Classify this cell by malaria status.
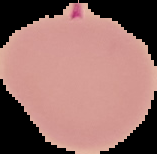

It is parasitized.

Summary:
  - Preparation: thin blood smear
  - Image size: 157×154 pixels
  - Image type: segmented cell region with the area outside set to black